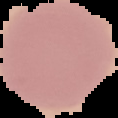
Image is 118×118 pixels. The area outside the segmented cell region is set to black. Malaria status: uninfected. From a thin blood film.